Assess this cell for malaria.
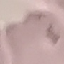
Uninfected.

Summary:
  - Capture: smartphone through the microscope eyepiece
  - Stain: Giemsa
  - Image type: automatically extracted cell patch, resized to 64 × 64 pixels
  - Preparation: thin smear